Assess this cell for malaria.
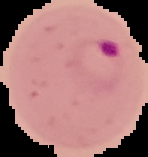

It is parasitized.

image type = segmented cell region on a black background
image size = 148×157 pixels
preparation = thin blood smear